Classify this cell by malaria status.
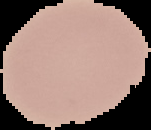
It is uninfected.

From a thin blood film. Segmented cell region on a black background. Image is 151×130 pixels.